Outline each blood parasite and name the species.
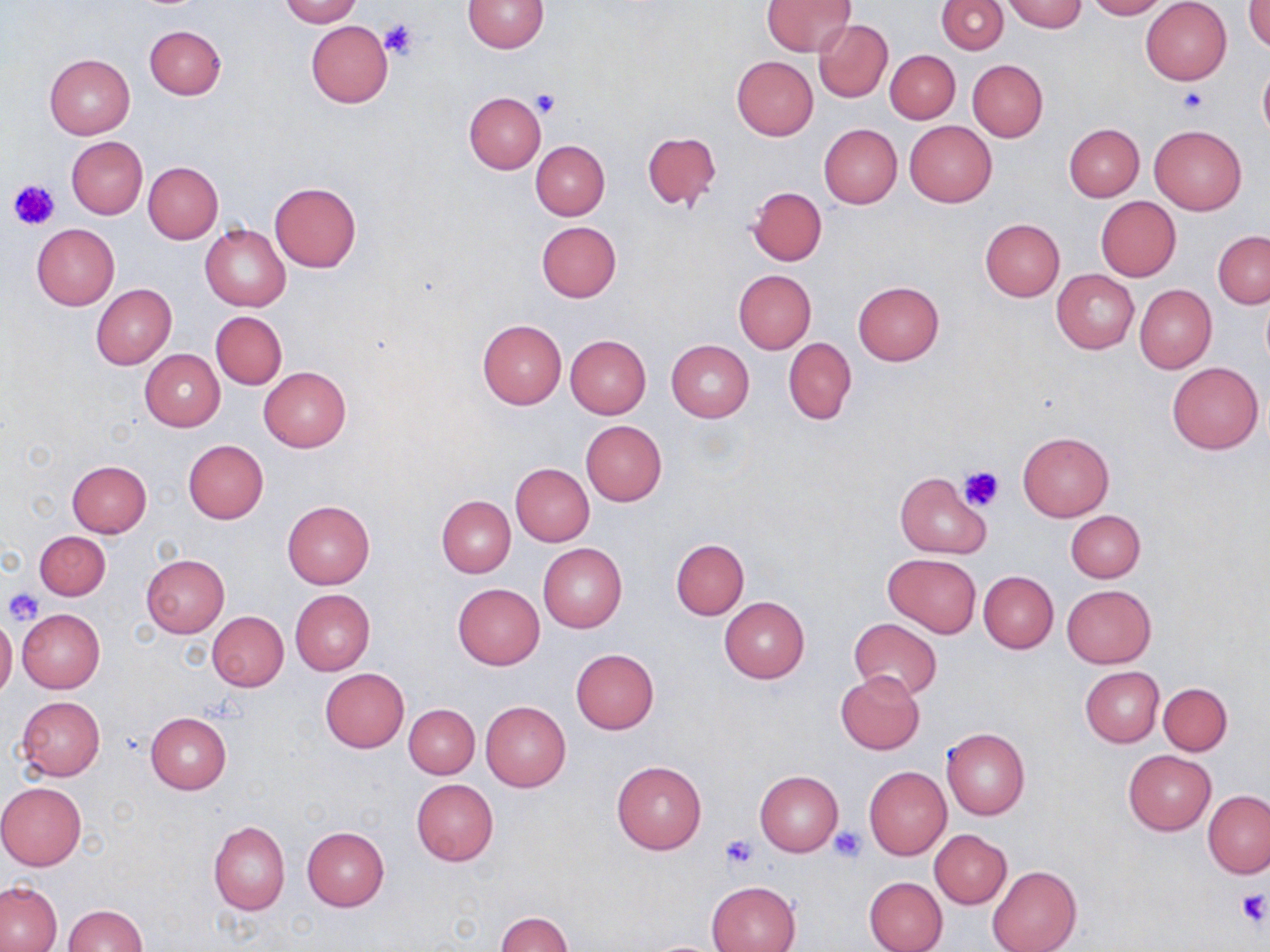
No blood parasites seen.

Approximate bounding boxes as [x1, y1, x2, y2] in pixels. Uninfected red blood cell locations: [281, 0, 360, 26], [462, 0, 547, 53], [938, 0, 1008, 53], [1004, 0, 1085, 33], [1085, 0, 1168, 20], [762, 1, 855, 57], [1141, 1, 1232, 85], [1247, 2, 1270, 52], [305, 19, 393, 108], [814, 20, 892, 103], [145, 25, 226, 99], [885, 50, 961, 123], [44, 54, 136, 138], [732, 56, 817, 139], [967, 59, 1047, 141], [1258, 62, 1270, 143], [464, 92, 545, 174], [905, 121, 997, 207], [819, 123, 902, 208], [1065, 123, 1144, 201], [1149, 124, 1247, 215], [642, 131, 722, 210], [66, 137, 147, 219], [531, 141, 609, 220], [144, 162, 223, 243], [269, 181, 360, 271], [749, 186, 826, 265], [1096, 197, 1181, 280], [979, 218, 1065, 301], [536, 221, 621, 302], [32, 224, 120, 309], [200, 224, 290, 311], [1213, 231, 1270, 309], [1052, 269, 1139, 354], [732, 270, 815, 354], [853, 281, 944, 364], [91, 283, 176, 369], [1134, 285, 1216, 373], [210, 311, 287, 390], [477, 319, 567, 408], [565, 335, 651, 418], [783, 337, 856, 425], [666, 340, 755, 421], [139, 349, 225, 431], [1166, 361, 1264, 454], [259, 366, 351, 452], [581, 420, 666, 506], [1018, 431, 1114, 520], [183, 439, 268, 524], [66, 460, 152, 538], [511, 464, 594, 545], [894, 472, 990, 558], [436, 495, 516, 578], [283, 501, 375, 588], [1067, 510, 1145, 583], [34, 530, 111, 600], [671, 538, 749, 619], [538, 544, 628, 633], [883, 553, 981, 637], [140, 554, 230, 637], [978, 570, 1058, 652], [453, 583, 544, 670], [1061, 584, 1155, 667], [290, 590, 375, 675], [719, 597, 809, 683], [17, 609, 105, 692], [207, 612, 289, 691], [0, 617, 16, 698], [848, 618, 942, 700], [571, 648, 659, 734], [1080, 666, 1164, 747], [320, 668, 410, 753], [835, 671, 925, 755], [1158, 682, 1232, 755], [17, 696, 105, 782], [481, 700, 571, 791], [405, 704, 479, 778], [145, 713, 231, 793], [941, 727, 1030, 819], [1123, 750, 1216, 834], [612, 760, 708, 855], [864, 766, 951, 860], [755, 770, 842, 856], [411, 780, 498, 865], [0, 782, 87, 869], [1204, 791, 1270, 878], [208, 820, 290, 914], [302, 826, 389, 911], [929, 829, 1012, 908], [987, 865, 1081, 952], [864, 876, 948, 952], [705, 880, 801, 952], [0, 882, 61, 951], [62, 905, 146, 951], [498, 912, 573, 951]. Platelet locations: [378, 20, 421, 63], [1178, 88, 1207, 114], [531, 90, 561, 118], [9, 178, 60, 230], [959, 463, 1006, 510], [4, 587, 47, 626], [828, 826, 866, 861], [720, 834, 761, 871], [1234, 890, 1269, 927]. Slide-level diagnosis: negative for blood parasites. Light microscopy. Image is 1270×952 pixels. One field of a larger specimen. May-Grünwald-Giemsa stain. Captured at 1000x magnification. Thin blood smear.